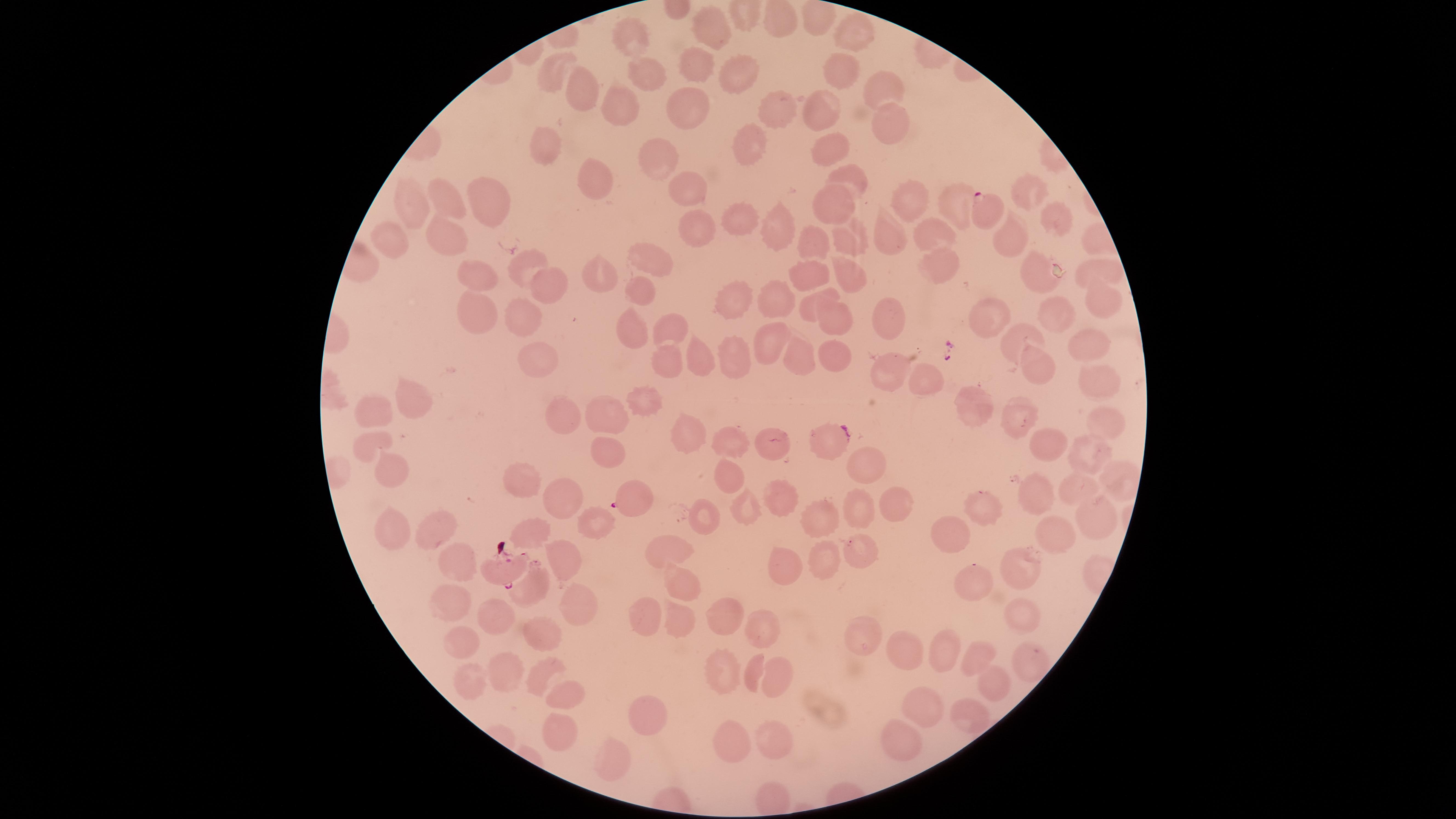
Approximate marker points as [x, y] in pixels.
Summary:
  - Uninfected RBCs: [816, 23], [778, 24], [708, 29], [852, 30], [630, 38], [651, 69], [844, 70], [696, 72], [551, 75], [741, 76], [882, 84], [584, 95], [779, 106], [622, 110], [828, 112], [688, 114], [889, 120], [748, 142], [550, 144], [832, 154], [662, 162], [596, 174], [849, 183], [691, 190], [1028, 192], [918, 201], [838, 205], [957, 205], [447, 207], [493, 208], [413, 209], [1051, 216], [698, 221], [737, 224], [776, 232], [395, 235], [455, 235], [890, 235], [934, 237], [852, 240], [1013, 240], [818, 246], [940, 257], [657, 260], [1088, 265], [525, 268], [1035, 270], [848, 271], [602, 272], [807, 273], [470, 276], [553, 284], [641, 291], [1104, 295], [824, 297], [772, 300], [737, 301], [478, 314], [533, 316], [835, 317], [993, 320], [1056, 321], [670, 323], [890, 323], [1011, 333], [632, 336], [776, 340], [1084, 345], [733, 355], [831, 355], [540, 359], [697, 359], [796, 359], [662, 361], [1038, 370], [1097, 371], [890, 374], [927, 377], [411, 393], [643, 400], [384, 405], [976, 407], [613, 414], [1019, 414], [563, 418], [1100, 423], [690, 430], [830, 436], [372, 438], [729, 442], [1043, 446], [1085, 452], [770, 454], [606, 456], [395, 469], [866, 471], [728, 476], [525, 478], [1078, 490], [564, 497], [773, 498], [1033, 498], [894, 500], [984, 508], [743, 512], [858, 515], [1095, 515], [820, 517], [704, 520], [601, 522], [397, 528], [439, 531], [533, 531], [1057, 535], [951, 538], [669, 552], [863, 552], [821, 559], [559, 561], [460, 563], [783, 569], [1022, 569], [977, 586], [535, 587], [680, 591], [568, 596], [453, 602], [1020, 612], [497, 613], [722, 614], [652, 616], [679, 625], [760, 626], [542, 632], [463, 640], [863, 643], [903, 647], [939, 650], [971, 655], [1025, 663], [506, 664], [723, 668], [540, 669], [755, 676], [468, 680], [773, 683], [992, 685], [560, 688], [922, 702], [643, 713], [969, 715], [558, 736], [903, 736], [768, 743], [726, 748], [611, 756]
  - Parasitized RBCs: [984, 212], [630, 499], [505, 571]
  - Image size: 1456×819 pixels
  - Stain: Giemsa
  - Field of view: single
  - Preparation: thin smear of blood
  - Visible region: circular
  - Capture: smartphone photograph through the microscope eyepiece
  - Species: Plasmodium falciparum
  - Presence: malaria parasites identified